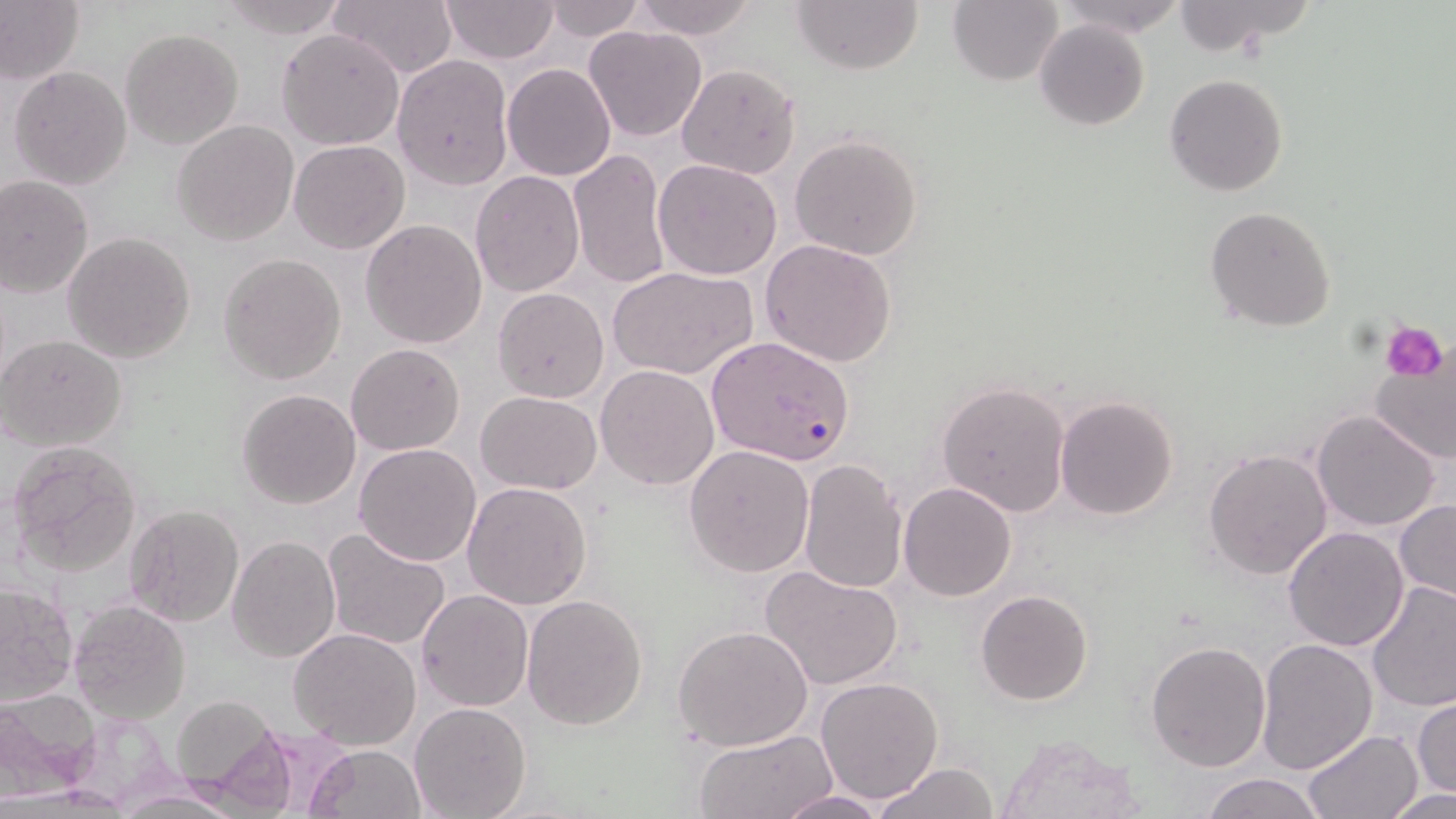
slide-level diagnosis = Plasmodium falciparum
preparation = thin blood film
uninfected red blood cell locations = approximate bounding boxes as [x1, y1, x2, y2] in pixels: [0, 0, 85, 88], [217, 0, 348, 37], [327, 0, 457, 80], [441, 0, 560, 66], [543, 0, 644, 40], [629, 0, 759, 40], [793, 0, 924, 73], [949, 0, 1064, 86], [1055, 0, 1185, 38], [1168, 0, 1317, 60], [1035, 20, 1149, 131], [584, 27, 708, 143], [120, 28, 243, 150], [277, 28, 404, 150], [392, 54, 513, 189], [676, 62, 802, 179], [502, 63, 617, 182], [7, 65, 132, 190], [1164, 74, 1289, 196], [172, 119, 299, 246], [791, 134, 923, 261], [289, 140, 411, 254], [567, 146, 671, 290], [652, 159, 783, 280], [470, 170, 585, 296], [0, 175, 94, 296], [1205, 206, 1338, 333], [361, 220, 487, 350], [62, 232, 196, 362], [758, 239, 898, 369], [219, 253, 347, 385], [609, 265, 759, 382], [492, 287, 610, 404], [0, 335, 126, 452], [1367, 337, 1456, 467], [345, 343, 466, 457], [596, 365, 719, 490], [938, 381, 1071, 516], [238, 390, 361, 509], [476, 391, 602, 492], [1053, 396, 1179, 520], [1311, 409, 1442, 532], [7, 440, 143, 576], [354, 443, 482, 568], [685, 443, 815, 576], [1204, 446, 1332, 581], [798, 457, 907, 595], [462, 481, 592, 610], [898, 482, 1017, 601], [1395, 501, 1456, 604], [126, 504, 244, 628], [1283, 525, 1409, 651], [321, 530, 451, 650], [228, 536, 340, 663], [759, 564, 905, 691], [1366, 581, 1456, 717], [1, 582, 78, 706], [417, 588, 533, 712], [975, 589, 1094, 705], [521, 594, 648, 731], [67, 601, 191, 725], [674, 625, 812, 753], [289, 628, 422, 749], [1257, 639, 1378, 773], [1146, 641, 1271, 771], [815, 677, 944, 803], [0, 690, 102, 793], [1412, 694, 1455, 798], [170, 695, 289, 803], [409, 702, 531, 818], [1302, 729, 1422, 817], [694, 730, 837, 819], [993, 731, 1144, 819], [307, 744, 427, 819], [873, 761, 999, 819], [1200, 772, 1328, 819], [1387, 787, 1452, 818], [776, 790, 888, 818]
magnification = 1000x
stain = May-Grünwald-Giemsa
modality = optical microscopy
image size = 1456×819 pixels
field of view = one of a larger specimen
Plasmodium falciparum-infected red blood cell locations = approximate bounding boxes as [x1, y1, x2, y2] in pixels: [707, 336, 854, 466]
platelet locations = approximate bounding boxes as [x1, y1, x2, y2] in pixels: [1381, 323, 1447, 383]